Outline each Plasmodium falciparum-infected red blood cell.
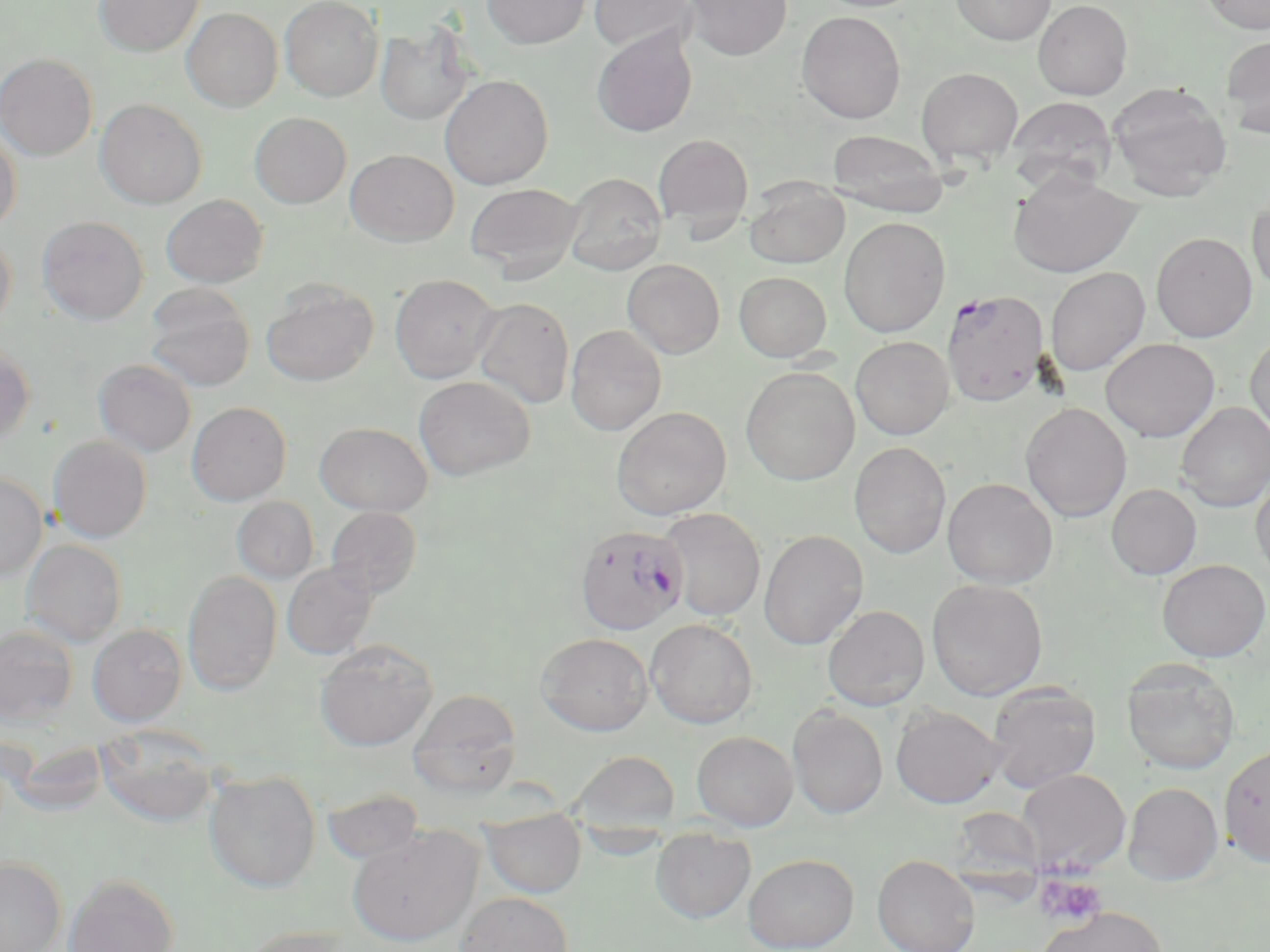

Approximate bounding boxes as named x1/y1/x2/y2 corners in pixels.
Plasmodium falciparum-infected red blood cells: (x1=942, y1=290, x2=1050, y2=406), (x1=576, y1=527, x2=690, y2=638).

slide_level_diagnosis: Plasmodium falciparum
image_size: 1270×952 pixels
stain: May-Grünwald-Giemsa
uninfected_red_blood_cell_locations: 'approximate bounding boxes as named x1/y1/x2/y2 corners in pixels: (x1=94, y1=0, x2=203, y2=57), (x1=279, y1=0, x2=383, y2=101), (x1=482, y1=0, x2=590, y2=49), (x1=588, y1=0, x2=698, y2=54), (x1=683, y1=0, x2=791, y2=60), (x1=951, y1=0, x2=1056, y2=45), (x1=1033, y1=0, x2=1132, y2=99), (x1=1199, y1=0, x2=1270, y2=34), (x1=181, y1=7, x2=283, y2=111), (x1=797, y1=11, x2=906, y2=123), (x1=375, y1=22, x2=475, y2=126), (x1=592, y1=27, x2=697, y2=137), (x1=1220, y1=35, x2=1270, y2=139), (x1=0, y1=53, x2=97, y2=161), (x1=917, y1=66, x2=1024, y2=166), (x1=439, y1=74, x2=554, y2=189), (x1=1106, y1=82, x2=1231, y2=202), (x1=1005, y1=96, x2=1118, y2=191), (x1=95, y1=98, x2=207, y2=209), (x1=250, y1=112, x2=351, y2=208), (x1=0, y1=127, x2=22, y2=231), (x1=825, y1=130, x2=950, y2=215), (x1=653, y1=133, x2=753, y2=234), (x1=346, y1=149, x2=458, y2=246), (x1=1007, y1=170, x2=1141, y2=278), (x1=563, y1=173, x2=667, y2=275), (x1=744, y1=180, x2=849, y2=268), (x1=465, y1=182, x2=583, y2=278), (x1=161, y1=194, x2=268, y2=288), (x1=1247, y1=195, x2=1270, y2=294), (x1=37, y1=215, x2=148, y2=324), (x1=838, y1=217, x2=950, y2=338), (x1=0, y1=230, x2=16, y2=334), (x1=1151, y1=232, x2=1257, y2=342), (x1=622, y1=259, x2=724, y2=358), (x1=1045, y1=266, x2=1150, y2=376), (x1=733, y1=271, x2=831, y2=361), (x1=390, y1=273, x2=501, y2=383), (x1=262, y1=280, x2=379, y2=386), (x1=144, y1=284, x2=255, y2=391), (x1=472, y1=296, x2=575, y2=408), (x1=565, y1=325, x2=666, y2=435), (x1=1245, y1=331, x2=1270, y2=444), (x1=850, y1=336, x2=954, y2=439), (x1=1100, y1=338, x2=1220, y2=442), (x1=0, y1=342, x2=35, y2=446), (x1=93, y1=358, x2=197, y2=456), (x1=741, y1=366, x2=860, y2=485), (x1=414, y1=376, x2=534, y2=480), (x1=187, y1=402, x2=291, y2=505), (x1=1176, y1=402, x2=1270, y2=512), (x1=1020, y1=403, x2=1132, y2=522), (x1=611, y1=406, x2=731, y2=520), (x1=314, y1=421, x2=433, y2=516), (x1=48, y1=435, x2=152, y2=542), (x1=849, y1=442, x2=952, y2=558), (x1=0, y1=471, x2=47, y2=580), (x1=1251, y1=472, x2=1270, y2=583), (x1=942, y1=477, x2=1058, y2=589), (x1=1106, y1=484, x2=1202, y2=580), (x1=232, y1=497, x2=319, y2=583), (x1=325, y1=506, x2=422, y2=599), (x1=658, y1=508, x2=766, y2=621), (x1=758, y1=530, x2=868, y2=650), (x1=22, y1=539, x2=127, y2=647), (x1=1157, y1=559, x2=1269, y2=661), (x1=282, y1=562, x2=378, y2=659), (x1=182, y1=570, x2=282, y2=695), (x1=926, y1=578, x2=1048, y2=700), (x1=822, y1=605, x2=929, y2=710), (x1=645, y1=618, x2=758, y2=728), (x1=87, y1=624, x2=187, y2=726), (x1=0, y1=625, x2=79, y2=726), (x1=536, y1=633, x2=653, y2=735), (x1=315, y1=639, x2=437, y2=751), (x1=1122, y1=659, x2=1241, y2=775), (x1=986, y1=681, x2=1101, y2=792), (x1=409, y1=690, x2=523, y2=795), (x1=788, y1=705, x2=889, y2=820), (x1=890, y1=705, x2=1005, y2=808), (x1=95, y1=727, x2=220, y2=828), (x1=692, y1=731, x2=798, y2=831), (x1=1219, y1=743, x2=1270, y2=868), (x1=569, y1=750, x2=681, y2=833), (x1=1017, y1=769, x2=1130, y2=874), (x1=204, y1=770, x2=321, y2=892), (x1=1123, y1=782, x2=1224, y2=885), (x1=320, y1=787, x2=425, y2=866), (x1=958, y1=806, x2=1053, y2=904), (x1=481, y1=808, x2=586, y2=898), (x1=348, y1=825, x2=482, y2=946), (x1=650, y1=827, x2=756, y2=924), (x1=744, y1=852, x2=859, y2=952), (x1=872, y1=854, x2=979, y2=952), (x1=0, y1=857, x2=67, y2=952), (x1=63, y1=873, x2=179, y2=952), (x1=454, y1=891, x2=574, y2=952), (x1=1036, y1=906, x2=1169, y2=952), (x1=236, y1=925, x2=356, y2=952)'
platelet_locations: 'approximate bounding boxes as named x1/y1/x2/y2 corners in pixels: (x1=1034, y1=873, x2=1107, y2=927)'
preparation: thin blood smear
field_of_view: one of a larger specimen
magnification: 1000x
modality: light microscopy